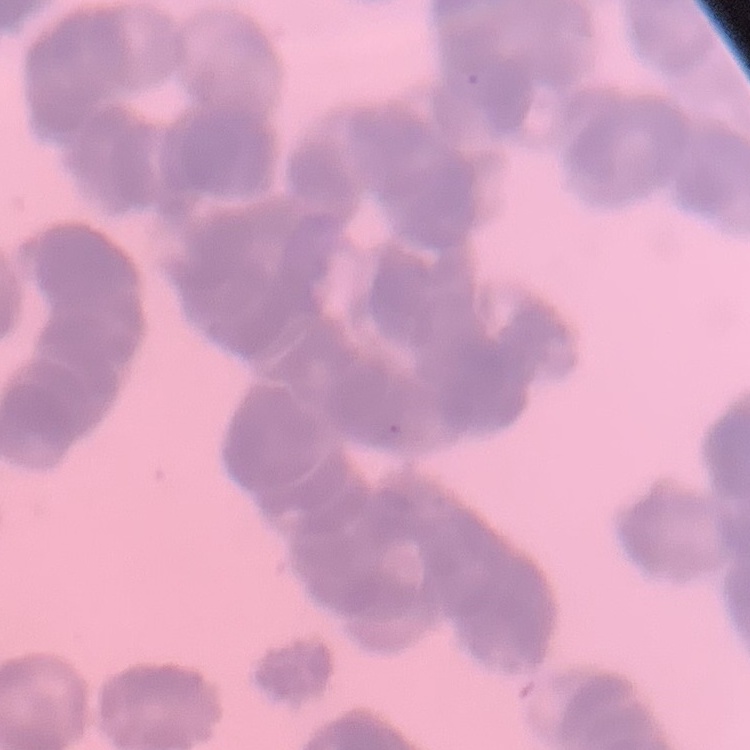
erythrocyte morphology = rouleaux formation
image type = one tile cut from a larger photomicrograph
preparation = thin peripheral smear
stain = Field's or Giemsa